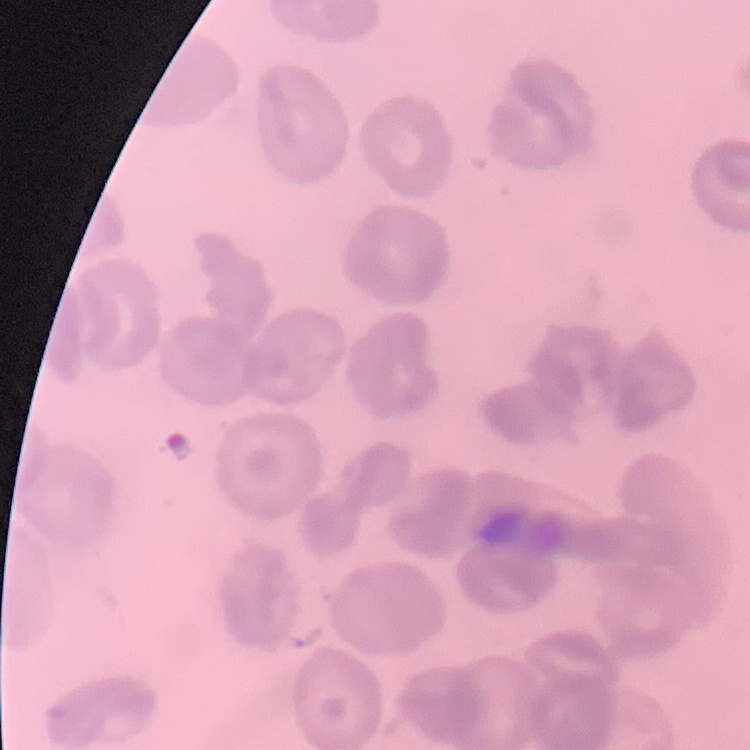
Summary:
  - Erythrocyte morphology: no rouleaux formation
  - Preparation: thin blood film
  - Image type: one tile cut from a larger photomicrograph
  - Stain: Field's or Giemsa